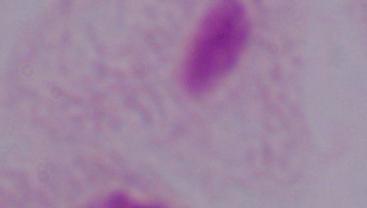
magnification = 1000x
identification = trichomonad
modality = photomicrograph